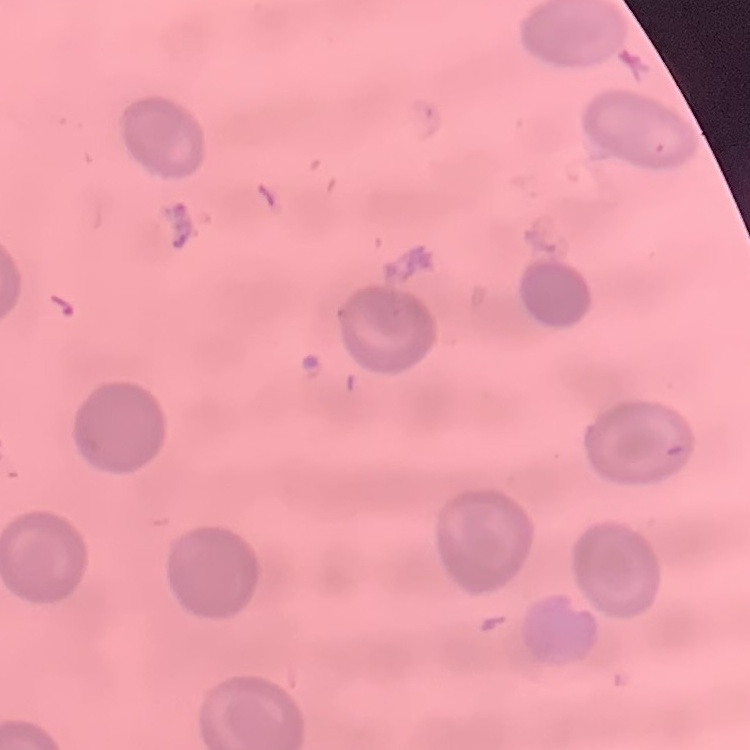
erythrocyte morphology = no rouleaux formation
stain = Field's or Giemsa
image type = one tile cut from a larger photomicrograph
preparation = thin peripheral smear